Outline each Plasmodium parasite.
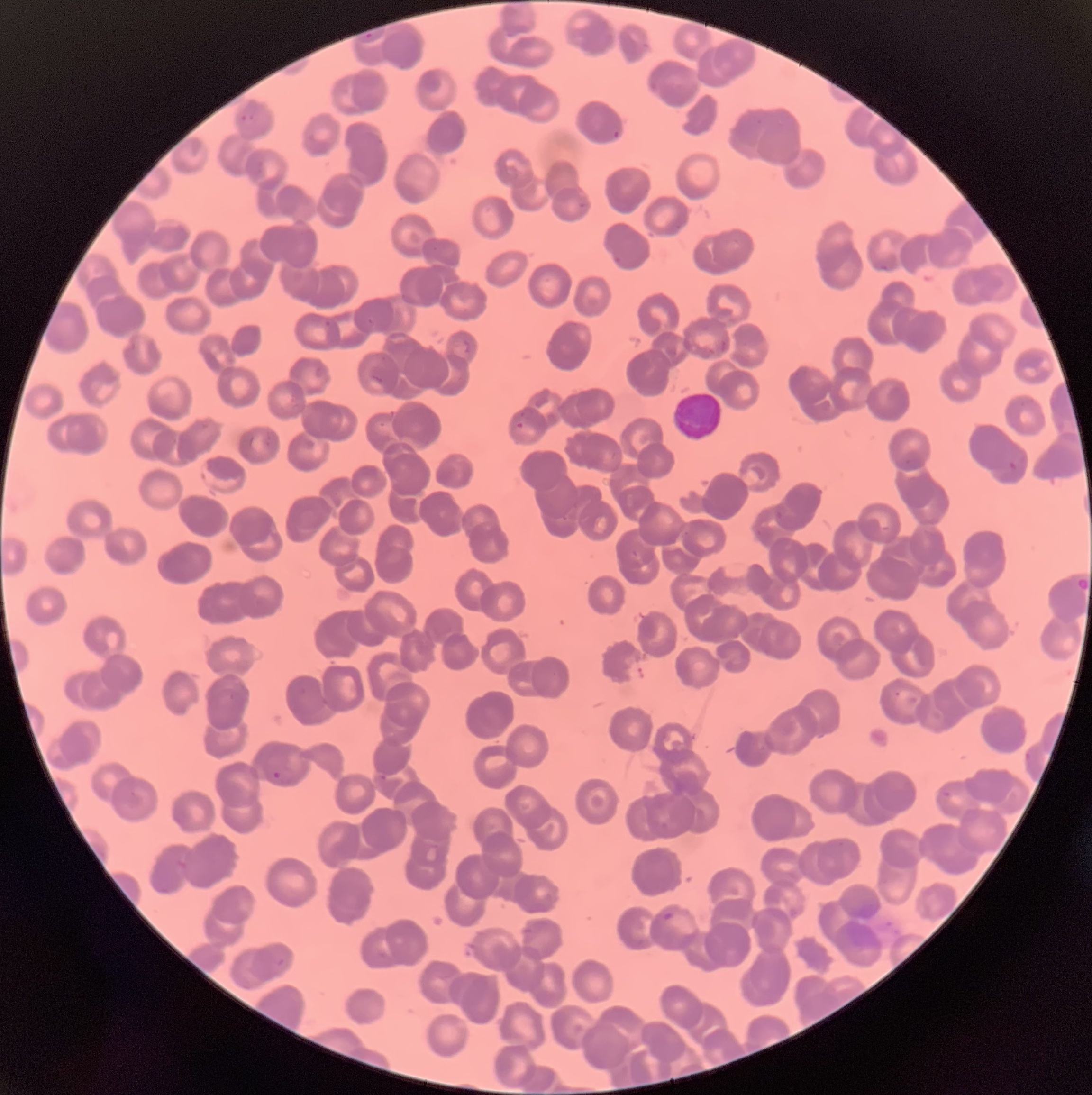

Approximate bounding boxes as named x1/y1/x2/y2 corners in pixels.
Plasmodium parasites: (x1=364, y1=32, x2=374, y2=41), (x1=239, y1=99, x2=260, y2=123), (x1=612, y1=129, x2=621, y2=139), (x1=514, y1=421, x2=525, y2=432), (x1=1008, y1=461, x2=1019, y2=472), (x1=1074, y1=575, x2=1092, y2=594), (x1=273, y1=771, x2=282, y2=780), (x1=663, y1=912, x2=674, y2=921).

White blood cell locations: (x1=671, y1=389, x2=725, y2=443). Thin blood film. Optical microscopy. Image is 1092×1095 pixels. The red blood cells show rouleaux formation.